Identify the cell.
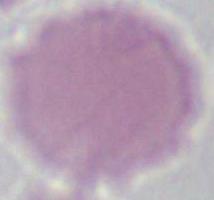
An erythrocyte.

Summary:
  - Modality: photomicrograph
  - Magnification: 1000x